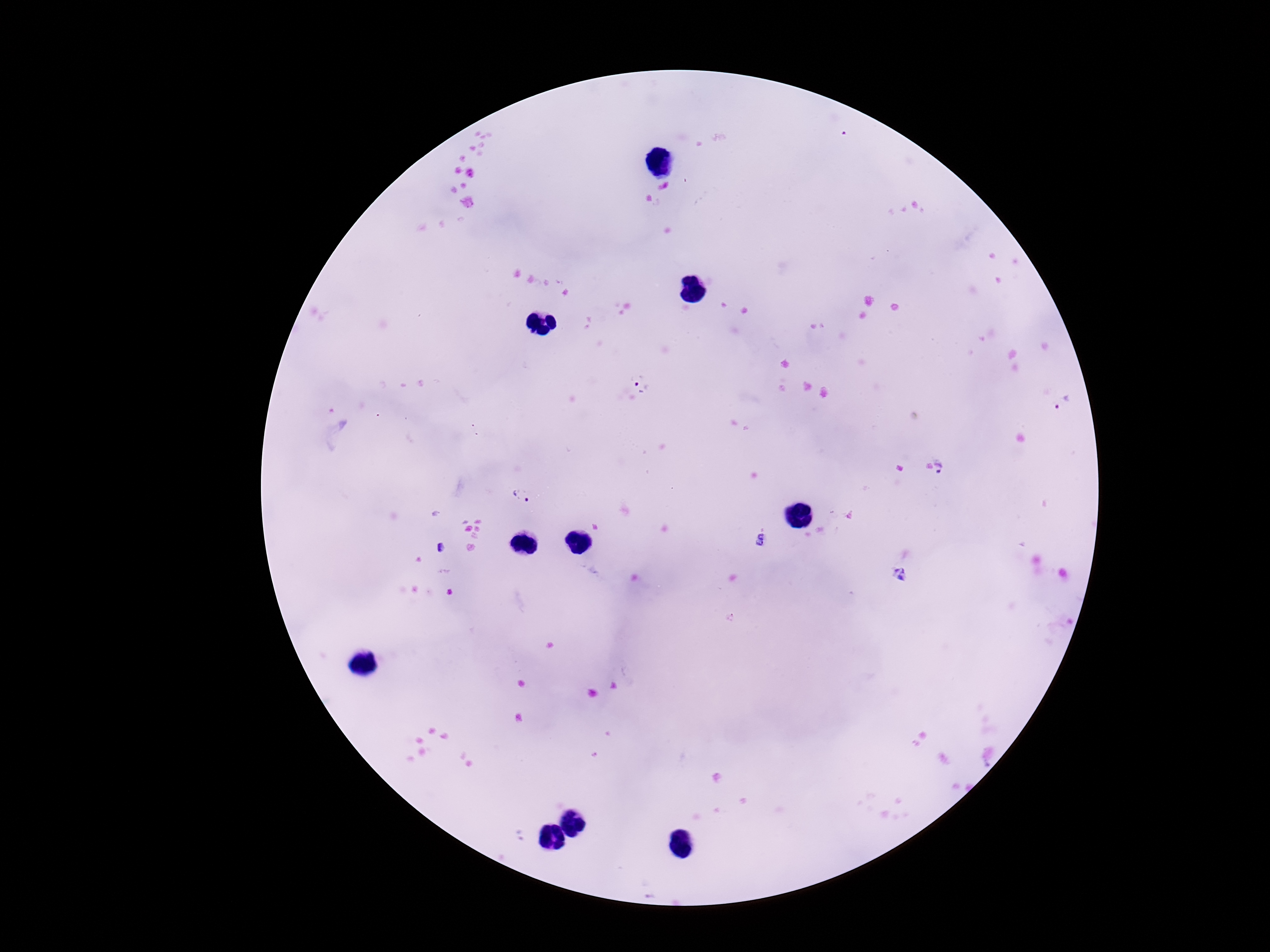
{
  "plasmodium_parasite_locations": "approximate object centers, in pixels from the top-left corner: (x=641, y=388), (x=1067, y=405), (x=945, y=467), (x=525, y=496), (x=760, y=540), (x=440, y=548), (x=901, y=577)",
  "patient_malaria_status": "positive",
  "field_of_view": "one from this slide",
  "image_size": "1270×952 pixels",
  "stain": "Giemsa",
  "capture": "smartphone camera through the microscope eyepiece",
  "preparation": "thick blood smear",
  "magnification": "100x"
}